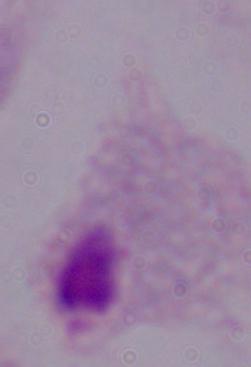

1000x magnification. A trichomonad is seen. Photomicrograph.